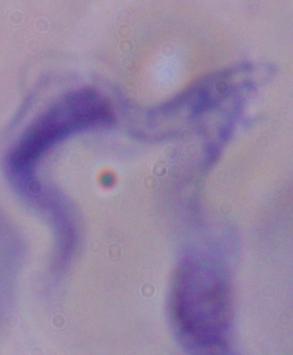
1000x magnification. A trypanosome is seen. Micrograph.